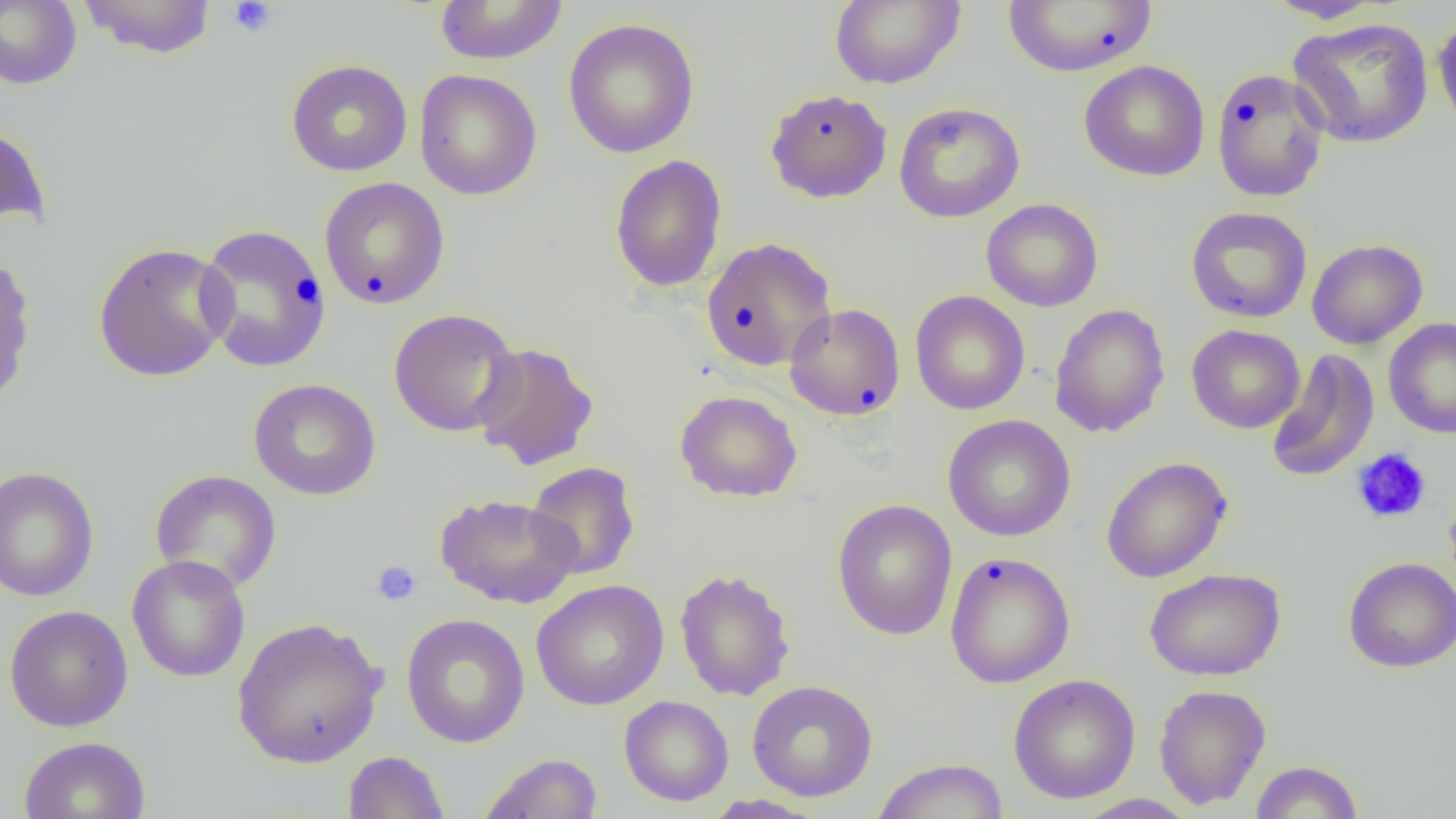 Approximate bounding boxes as [x1, y1, x2, y2] in pixels. Platelet locations: [228, 0, 277, 37], [1351, 447, 1432, 524], [371, 560, 421, 606]. Uninfected red blood cell locations: [0, 0, 82, 89], [78, 0, 218, 58], [433, 0, 568, 65], [829, 0, 965, 89], [1263, 0, 1387, 24], [1003, 1, 1157, 76], [1433, 11, 1456, 138], [1288, 17, 1434, 148], [563, 18, 700, 158], [285, 59, 413, 177], [1079, 60, 1210, 182], [1211, 67, 1330, 203], [414, 69, 542, 200], [765, 88, 892, 204], [893, 102, 1025, 223], [0, 121, 51, 230], [610, 154, 727, 292], [319, 177, 450, 310], [980, 198, 1104, 312], [1186, 206, 1312, 323], [195, 223, 332, 372], [700, 236, 837, 372], [1307, 238, 1428, 349], [92, 242, 233, 382], [0, 250, 37, 406], [910, 290, 1029, 415], [784, 303, 905, 421], [1049, 303, 1170, 438], [388, 308, 522, 438], [1383, 317, 1456, 439], [1187, 324, 1304, 433], [471, 342, 599, 471], [1265, 349, 1380, 484], [248, 378, 381, 500], [675, 390, 802, 502], [942, 414, 1076, 541], [1101, 456, 1232, 583], [526, 461, 640, 581], [0, 465, 100, 602], [149, 469, 282, 595], [1444, 488, 1456, 597], [435, 493, 580, 608], [831, 499, 958, 640], [944, 552, 1076, 688], [127, 554, 251, 683], [1342, 556, 1456, 673], [1145, 567, 1286, 681], [675, 568, 795, 701], [530, 579, 669, 710], [4, 605, 133, 731], [401, 613, 529, 748], [231, 616, 388, 768], [1008, 673, 1140, 804], [747, 679, 878, 801], [1153, 684, 1271, 810], [619, 695, 734, 806], [19, 736, 151, 819], [343, 751, 449, 818], [479, 752, 603, 819], [870, 758, 1009, 819], [1250, 760, 1364, 818], [1072, 793, 1199, 818], [701, 794, 825, 818]. Slide-level diagnosis: negative for blood parasites. One field of a larger specimen. Image is 1456×819 pixels. Light microscopy. Captured at 1000x magnification. Thin blood smear.